Identify the parasite.
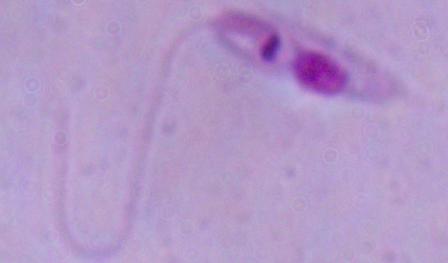
Leishmania.

1000x magnification. Photomicrograph.